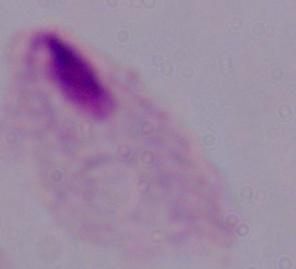

Summary:
  - Modality: photomicrograph
  - Magnification: 1000x
  - Identification: trichomonad